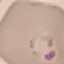
Result: malaria parasites identified. Giemsa-stained preparation. Thin smear of blood. Acquired by smartphone through the microscope eyepiece. Cell patch, automatically extracted from a larger field of view and resized to 64 × 64 pixels.